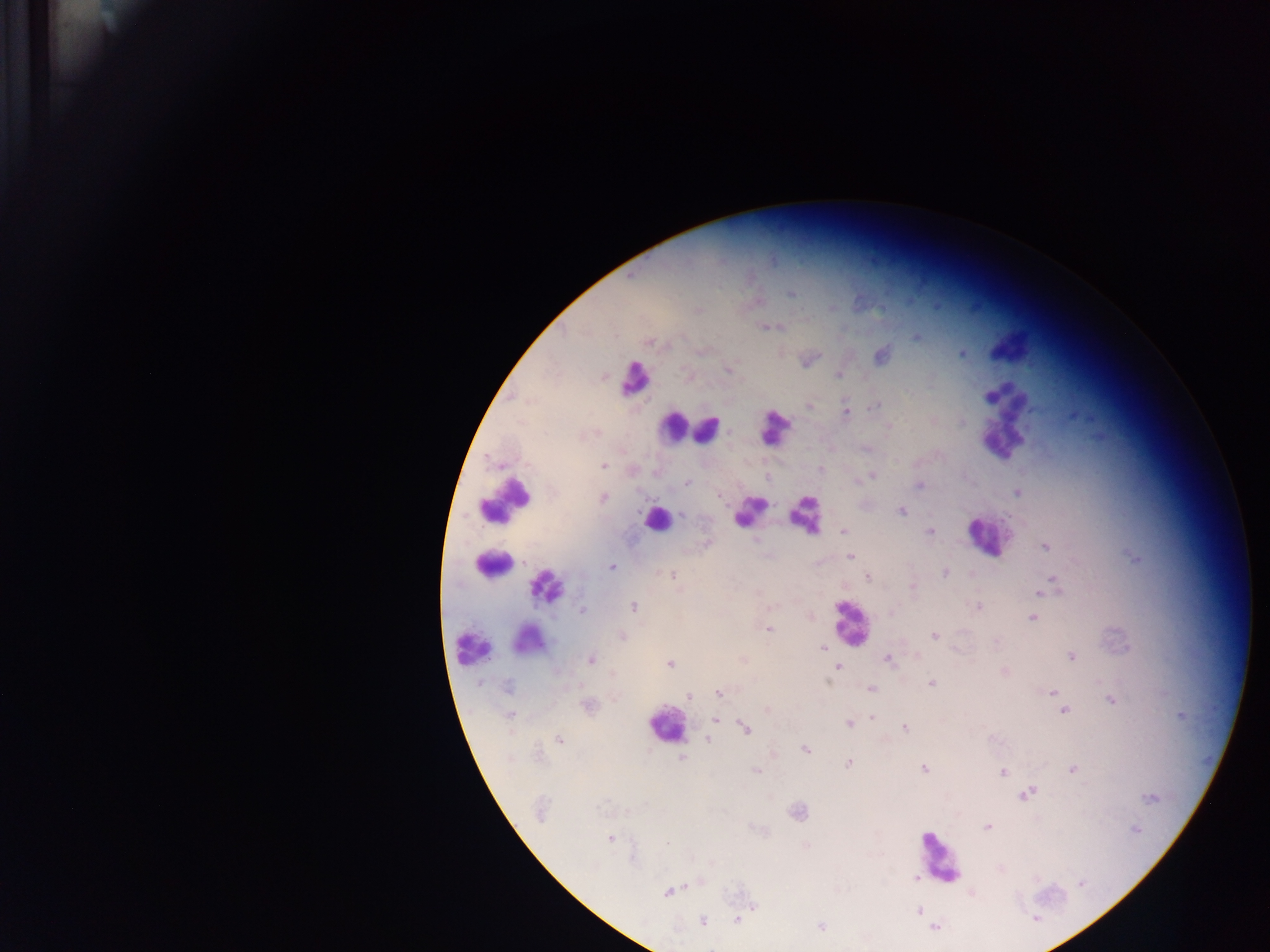

Approximate centers as {x, y} in pixels.
Summary:
  - Plasmodium parasite locations: {632, 275}, {792, 293}, {698, 310}, {764, 326}, {918, 337}, {650, 342}, {703, 351}, {962, 353}, {880, 355}, {728, 371}, {838, 375}, {809, 405}, {874, 405}, {845, 412}, {888, 426}, {603, 466}, {821, 469}, {871, 476}, {686, 483}, {919, 485}, {1018, 493}, {721, 497}, {603, 499}, {901, 511}, {682, 514}, {843, 531}, {929, 532}, {757, 539}, {706, 544}, {1045, 547}, {851, 557}, {1136, 558}, {612, 567}, {945, 573}, {671, 576}, {868, 577}, {1054, 580}, {1047, 586}, {912, 587}, {1040, 593}, {634, 606}, {978, 606}, {582, 611}, {890, 611}, {1032, 618}, {768, 629}, {935, 636}, {622, 637}, {995, 641}, {822, 648}, {1071, 656}, {887, 659}, {591, 660}, {743, 660}, {670, 664}, {838, 667}, {1005, 672}, {931, 683}, {508, 687}, {871, 689}, {1052, 692}, {719, 693}, {689, 697}, {1111, 701}, {588, 706}, {1063, 711}, {1181, 715}, {510, 716}, {871, 717}, {715, 720}, {848, 724}, {745, 728}, {904, 728}, {558, 739}, {707, 740}, {805, 749}, {682, 758}, {849, 763}, {924, 769}, {1073, 769}, {757, 771}, {1003, 771}, {1026, 793}, {1150, 799}, {627, 810}, {540, 812}, {797, 812}, {987, 826}, {1136, 830}, {610, 840}, {667, 844}, {806, 846}, {915, 876}, {1080, 883}, {668, 891}, {754, 907}, {918, 911}, {1035, 919}, {736, 920}, {702, 922}, {821, 927}, {935, 927}
  - Leukocyte locations: {1006, 348}, {635, 379}, {1006, 419}, {774, 425}, {674, 428}, {708, 430}, {505, 501}, {748, 512}, {804, 514}, {656, 520}, {988, 537}, {492, 564}, {547, 586}, {846, 622}, {524, 636}, {469, 648}, {665, 725}, {938, 858}
  - Image size: 1270×952 pixels
  - Preparation: thick blood film
  - Field of view: single
  - Capture: mobile-phone photograph through a microscope
  - Country: Ghana